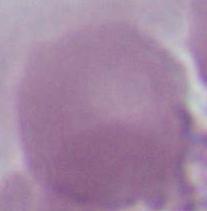 Captured at 1000x magnification. A red blood cell is seen. Micrograph.